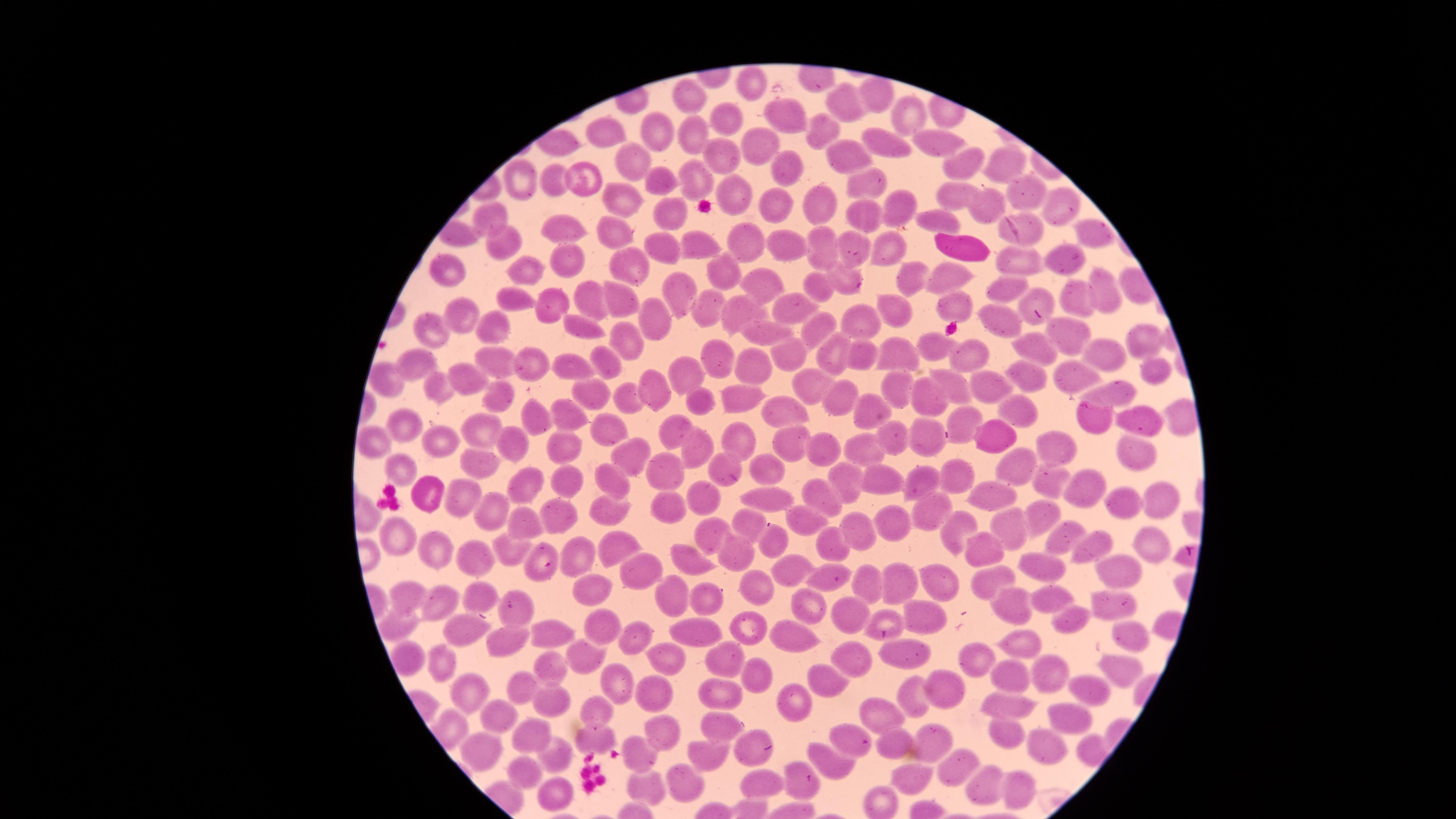 Approximate marker points as (x, y) in pixels. White blood cells: (956, 247). Uninfected red blood cells: (749, 82), (881, 96), (694, 99), (839, 107), (905, 115), (787, 116), (724, 122), (815, 125), (654, 133), (691, 134), (606, 135), (884, 141), (942, 141), (760, 143), (842, 153), (716, 157), (628, 159), (997, 160), (959, 166), (788, 167), (590, 177), (697, 177), (521, 178), (661, 180), (868, 180), (555, 184), (729, 190), (621, 193), (952, 193), (1025, 194), (817, 199), (989, 204), (1062, 204), (776, 205), (900, 205), (674, 215), (864, 215), (931, 217), (494, 222), (566, 224), (1092, 229), (616, 232), (1025, 235), (503, 240), (747, 243), (662, 245), (823, 245), (850, 245), (695, 246), (894, 248), (787, 252), (1018, 258), (1059, 263), (570, 264), (631, 266), (727, 267), (904, 268), (446, 269), (526, 272), (952, 276), (1102, 276), (759, 280), (840, 280), (825, 283), (1004, 287), (677, 288), (1075, 297), (512, 298), (590, 299), (1033, 299), (621, 302), (952, 303), (551, 305), (709, 305), (794, 306), (897, 309), (742, 310), (458, 314), (658, 321), (1001, 321), (862, 322), (580, 326), (488, 330), (818, 331), (765, 332), (434, 333), (1066, 333), (626, 339), (1144, 340), (927, 345), (970, 351), (1033, 351), (836, 352), (1099, 352), (892, 355), (787, 356), (603, 358), (858, 360), (717, 361), (419, 366), (500, 366), (530, 366), (571, 368), (1153, 368), (759, 369), (1031, 375), (1069, 375), (686, 377), (807, 380), (465, 382), (390, 383), (654, 385), (952, 386), (896, 387), (989, 387), (1121, 389), (440, 391), (595, 392), (498, 395), (733, 395), (843, 397), (924, 397), (626, 398), (702, 401), (1017, 408), (869, 411), (789, 412), (561, 414), (530, 418), (963, 419), (1140, 421), (401, 425), (480, 426), (608, 432), (673, 432), (926, 435), (891, 436), (991, 437), (440, 438), (512, 438), (736, 439), (791, 443), (372, 444), (697, 446), (1058, 446), (565, 447), (829, 448), (863, 451), (623, 453), (1134, 453), (1018, 457), (769, 465), (719, 467), (405, 468), (958, 474), (478, 475), (667, 476), (881, 476), (921, 477), (845, 478), (530, 479), (566, 480), (614, 480), (1048, 481), (1087, 486), (426, 493), (456, 494), (821, 494), (991, 496), (701, 499), (1161, 500), (766, 502), (667, 503), (1119, 505), (606, 508), (481, 510), (932, 510), (555, 516), (1048, 517), (745, 520), (806, 520), (524, 522), (896, 524), (1012, 529), (859, 532), (956, 533), (709, 534), (1059, 538), (772, 540), (610, 542), (983, 542), (837, 543), (396, 544), (1150, 545), (1094, 547), (538, 553), (438, 554), (512, 555), (738, 555), (686, 559), (477, 560), (571, 560), (1040, 564), (1124, 568), (641, 569), (789, 571), (829, 577), (987, 577), (937, 579), (865, 583), (584, 584), (757, 585), (896, 585), (679, 592), (480, 593), (1049, 595), (409, 596), (711, 597), (1116, 606), (443, 607), (813, 608), (849, 612), (1015, 612), (515, 613), (924, 613), (1068, 617), (887, 621), (596, 623), (401, 625), (748, 628), (539, 631), (694, 632), (461, 633), (1124, 633), (502, 637), (786, 638), (1023, 640), (630, 644), (905, 648), (847, 654), (404, 657), (582, 657), (664, 659), (724, 659), (976, 660), (444, 661), (1114, 669), (546, 670), (1052, 673), (761, 676), (1012, 678), (619, 680), (832, 682), (522, 685), (944, 691), (654, 692), (718, 692), (468, 693), (1090, 693), (915, 696), (547, 699), (792, 702), (1009, 707), (600, 708), (493, 714), (885, 714), (1068, 718), (721, 728), (664, 733), (532, 736), (1003, 736), (596, 739), (851, 739), (930, 743), (899, 745), (478, 751), (1046, 751), (750, 752), (706, 755), (826, 756), (642, 757), (552, 760), (955, 768), (525, 772), (766, 783), (642, 784), (913, 784), (687, 785), (982, 785), (799, 787), (1011, 790), (549, 796). One field of view of the specimen. Presence: no malaria parasites detected. Circular visible region. Thin blood film. Giemsa stain. Image is 1456×819 pixels. Photographed with a smartphone camera through the microscope eyepiece.